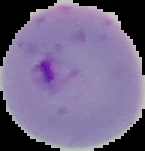

image size = 145×151 pixels
result = Plasmodium parasites detected
image type = cell region segmented out of the field of view; surrounding area masked to black
preparation = thin blood film